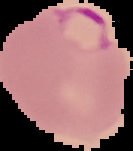

{
  "preparation": "thin blood smear",
  "image_size": "133×151 pixels",
  "malaria_status": "parasitized",
  "image_type": "cell region segmented out of the field of view; surrounding area masked to black"
}